Classify this cell by malaria status.
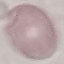

Uninfected.

Thin blood smear. Cell patch, automatically extracted from a larger field of view and resized to 64 × 64 pixels. Giemsa-stained preparation. Photographed with a smartphone camera at the microscope eyepiece.